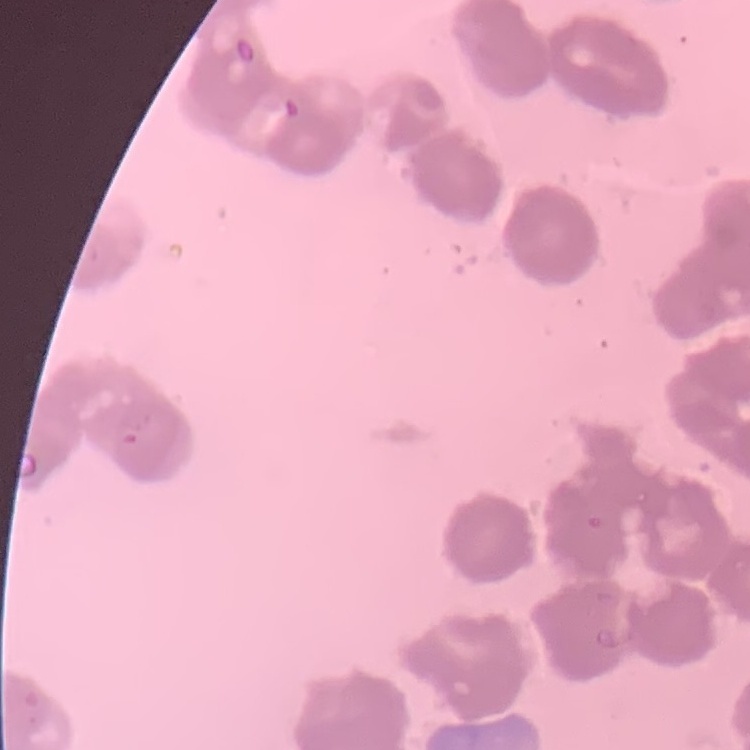

The red blood cells show rouleaux formation. One tile cut from a larger photomicrograph. Field's or Giemsa stain. Thin blood smear.